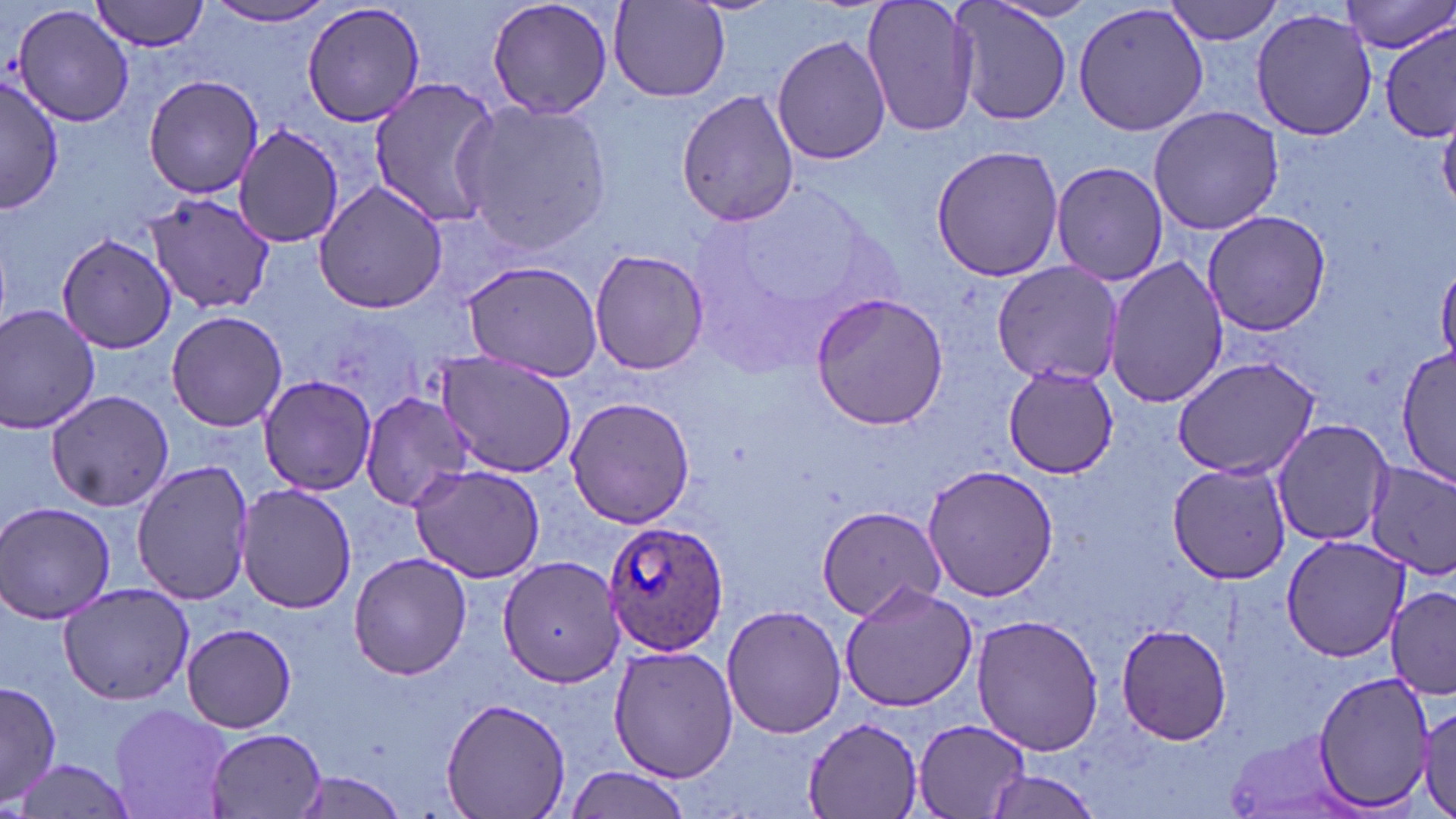

slide-level diagnosis = Plasmodium ovale
image size = 1456×819 pixels
field of view = single
stain = May-Grünwald-Giemsa
preparation = thin blood smear
modality = light microscopy
Plasmodium ovale-infected red blood cell locations = approximate bounding boxes as (x1, y1, x2, y2) in pixels: (601, 520, 730, 656)
magnification = 1000x
uninfected red blood cell locations = approximate bounding boxes as (x1, y1, x2, y2) in pixels: (92, 0, 213, 52), (484, 0, 616, 121), (860, 0, 982, 138), (1163, 0, 1285, 45), (301, 1, 426, 128), (1343, 1, 1453, 55), (202, 2, 340, 27), (610, 2, 731, 101), (950, 2, 1070, 126), (1072, 2, 1210, 137), (12, 4, 136, 128), (1251, 8, 1378, 141), (1378, 25, 1455, 141), (771, 34, 890, 166), (143, 74, 262, 199), (1, 75, 64, 213), (365, 76, 507, 227), (676, 88, 799, 229), (454, 99, 613, 255), (1148, 105, 1283, 235), (234, 125, 345, 245), (930, 143, 1064, 283), (1050, 161, 1169, 285), (314, 180, 448, 314), (134, 189, 275, 317), (1201, 210, 1330, 336), (56, 232, 178, 354), (588, 248, 708, 376), (1104, 258, 1229, 410), (461, 260, 602, 379), (993, 261, 1122, 386), (810, 292, 952, 431), (0, 305, 101, 434), (165, 311, 289, 431), (1397, 346, 1456, 490), (432, 353, 577, 479), (1171, 356, 1321, 480), (1000, 363, 1121, 479), (258, 374, 376, 496), (46, 390, 175, 513), (361, 393, 476, 512), (564, 396, 696, 528), (1269, 419, 1392, 548), (132, 460, 257, 604), (1366, 460, 1455, 579), (1167, 463, 1292, 585), (410, 464, 547, 584), (922, 464, 1061, 601), (237, 484, 357, 613), (0, 503, 120, 623), (816, 504, 950, 622), (1280, 533, 1413, 662), (348, 552, 472, 679), (499, 554, 624, 686), (58, 580, 193, 705), (839, 582, 978, 713), (1386, 583, 1456, 700), (720, 604, 846, 740), (971, 614, 1104, 756), (180, 621, 299, 732), (1114, 623, 1234, 745), (609, 643, 737, 782), (1313, 668, 1434, 813), (1, 681, 60, 807), (442, 696, 570, 819), (108, 702, 232, 819), (1416, 705, 1453, 816), (804, 717, 925, 817), (913, 717, 1030, 817), (204, 727, 328, 818), (1224, 729, 1359, 819), (15, 757, 135, 819), (564, 767, 693, 819), (975, 767, 1104, 816), (289, 772, 412, 818)